Locate and identify every blood parasite.
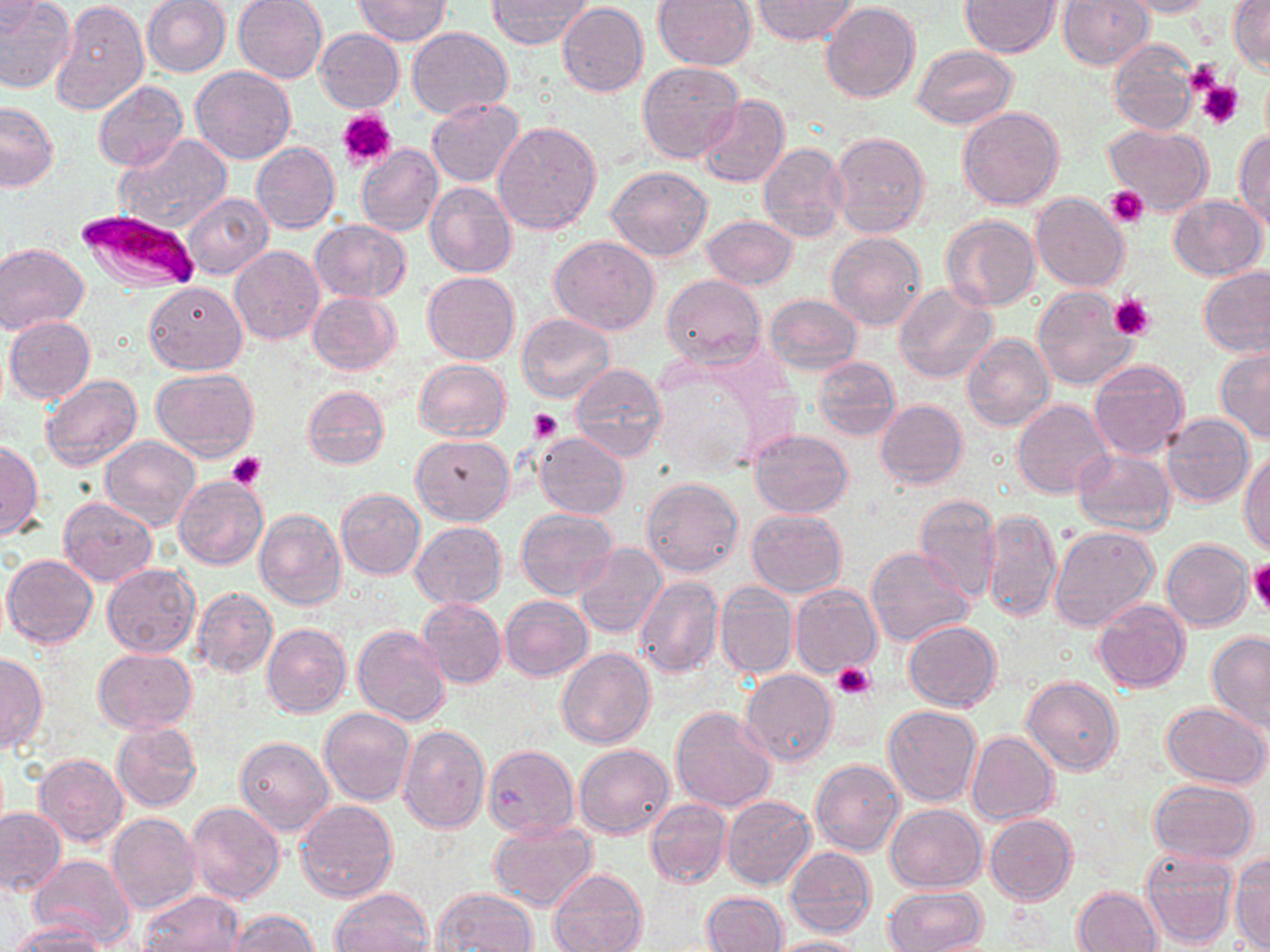
Approximate bounding boxes as (x1, y1, x2, y2) in pixels.
Plasmodium falciparum-infected red blood cells: (74, 207, 197, 291).
No Plasmodium ovale, Plasmodium malariae, Plasmodium vivax, Babesia divergens, or Trypanosoma brucei observed.

Summary:
  - Platelet locations: (1182, 61, 1224, 96), (1197, 80, 1243, 130), (339, 110, 397, 170), (1105, 185, 1148, 226), (1110, 293, 1156, 342), (530, 408, 561, 442), (227, 452, 267, 490), (1248, 558, 1270, 614), (833, 663, 875, 699)
  - Uninfected red blood cell locations: (0, 0, 76, 93), (233, 0, 328, 83), (352, 0, 451, 46), (751, 0, 858, 44), (961, 0, 1059, 56), (1118, 0, 1215, 18), (1228, 0, 1269, 75), (52, 1, 148, 116), (141, 1, 232, 77), (487, 1, 593, 48), (653, 1, 756, 71), (1057, 1, 1154, 70), (1, 2, 43, 38), (557, 2, 649, 97), (819, 2, 920, 104), (407, 27, 513, 119), (315, 29, 404, 112), (1108, 40, 1199, 136), (911, 44, 1017, 130), (638, 61, 745, 164), (191, 66, 296, 165), (92, 81, 188, 171), (697, 95, 790, 187), (427, 98, 524, 186), (0, 101, 58, 192), (957, 105, 1065, 210), (493, 122, 603, 235), (1103, 123, 1214, 217), (1233, 129, 1270, 228), (830, 131, 932, 237), (114, 134, 231, 234), (251, 142, 341, 233), (356, 143, 443, 237), (757, 144, 848, 244), (607, 165, 714, 262), (425, 180, 517, 278), (183, 193, 273, 279), (1032, 193, 1130, 292), (1168, 195, 1267, 280), (942, 214, 1040, 312), (701, 215, 795, 290), (686, 217, 786, 346), (310, 219, 410, 302), (827, 231, 927, 331), (549, 235, 660, 335), (0, 243, 89, 335), (230, 245, 324, 344), (1198, 266, 1270, 357), (422, 271, 520, 365), (663, 274, 765, 366), (144, 281, 248, 375), (893, 283, 998, 384), (1031, 287, 1139, 392), (308, 291, 401, 374), (764, 293, 863, 375), (517, 314, 615, 403), (4, 316, 96, 404), (962, 334, 1055, 434), (1215, 347, 1270, 441), (813, 357, 900, 440), (413, 358, 512, 443), (1087, 360, 1190, 460), (568, 363, 667, 460), (151, 368, 259, 460), (39, 374, 142, 473), (304, 386, 389, 469), (875, 399, 968, 490), (1012, 400, 1114, 499), (1161, 413, 1254, 507), (751, 429, 853, 516), (535, 433, 629, 519), (411, 434, 515, 525), (99, 436, 200, 530), (0, 439, 41, 542), (1239, 448, 1269, 553), (1074, 449, 1177, 537), (174, 477, 268, 570), (642, 478, 744, 578), (336, 488, 426, 580), (914, 492, 1001, 603), (58, 497, 157, 587), (516, 506, 617, 600), (253, 508, 346, 609), (746, 509, 847, 597), (983, 509, 1062, 621), (411, 522, 506, 608), (1049, 525, 1161, 632), (1162, 538, 1254, 630), (575, 543, 668, 639), (865, 547, 973, 650), (3, 554, 98, 650), (101, 563, 200, 658), (635, 576, 723, 678), (714, 583, 798, 679), (789, 584, 881, 678), (192, 587, 278, 678), (500, 596, 593, 681), (417, 597, 507, 688), (1093, 599, 1189, 693), (902, 620, 1000, 710), (262, 624, 351, 719), (353, 625, 452, 726), (1207, 631, 1270, 731), (557, 647, 655, 750), (92, 648, 198, 735), (0, 655, 46, 753), (741, 670, 837, 767), (1021, 675, 1122, 776), (1160, 701, 1269, 788), (671, 705, 776, 812), (883, 705, 982, 808), (319, 708, 416, 807), (111, 721, 202, 811), (397, 724, 491, 834), (966, 731, 1058, 825), (235, 737, 334, 837), (574, 743, 674, 839), (484, 744, 580, 840), (35, 753, 129, 847), (810, 757, 905, 856), (1148, 779, 1259, 865), (722, 796, 815, 888), (295, 799, 398, 904), (646, 799, 731, 888), (185, 802, 285, 905), (885, 804, 986, 893), (0, 807, 65, 896), (107, 812, 201, 915), (984, 813, 1078, 905), (488, 820, 598, 912), (786, 847, 876, 938), (1139, 847, 1237, 950), (1230, 852, 1270, 950), (30, 854, 134, 946), (547, 868, 649, 952), (328, 886, 436, 952), (884, 886, 988, 952), (434, 887, 538, 952), (1074, 887, 1162, 951), (703, 890, 787, 952), (141, 891, 245, 952), (226, 909, 321, 950), (14, 921, 108, 951), (766, 936, 867, 952)
  - Slide-level diagnosis: Plasmodium falciparum
  - Magnification: 1000x
  - Stain: May-Grünwald-Giemsa
  - Modality: light microscopy
  - Image size: 1270×952 pixels
  - Preparation: thin blood film
  - Field of view: one of a larger specimen